Comment on the morphology of the erythrocytes.
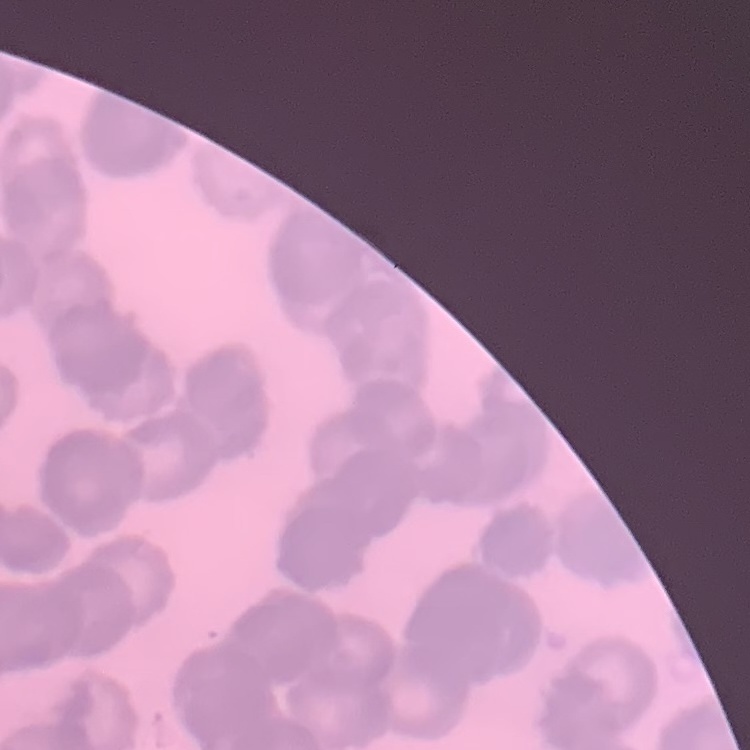
They show rouleaux formation.

image_type: one tile cut from a larger photomicrograph
preparation: thin peripheral smear
stain: Field's or Giemsa